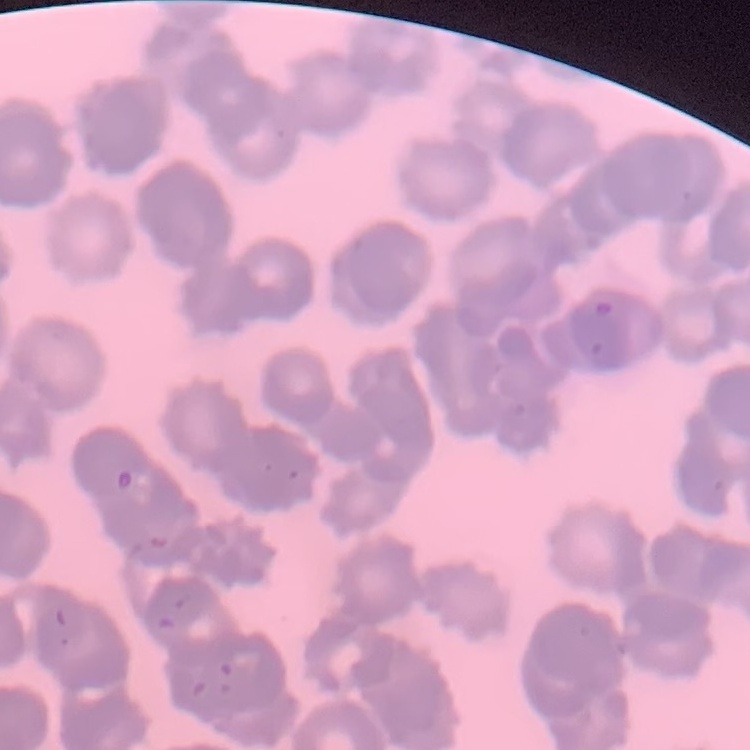

erythrocyte_morphology: rouleaux formation
stain: Field's or Giemsa
preparation: thin peripheral smear
image_type: square crop of a larger photomicrograph